Describe the morphology of the erythrocytes.
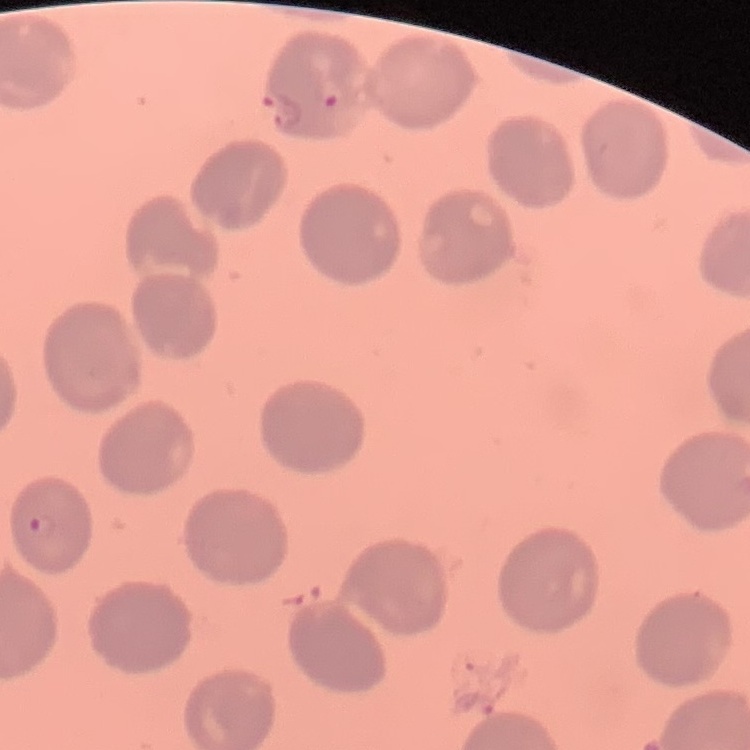
They show no rouleaux formation.

preparation = thin peripheral smear
stain = Field's or Giemsa
image type = one tile cut from a larger photomicrograph